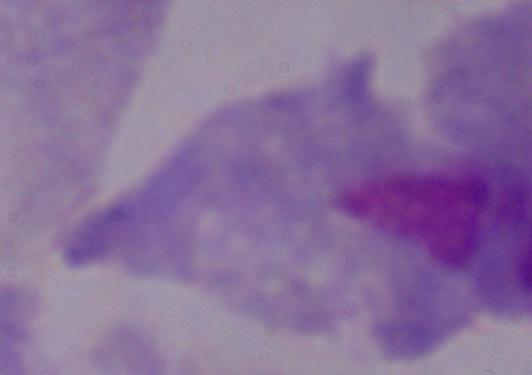

modality = micrograph
magnification = 1000x
identification = trichomonad